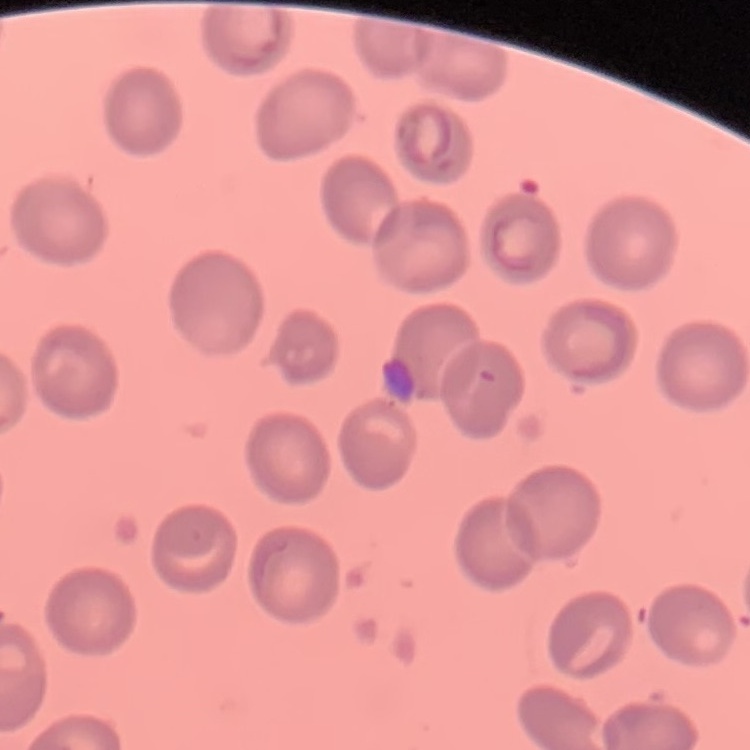

erythrocyte morphology = no rouleaux formation
stain = Field's or Giemsa
preparation = thin blood smear
image type = one tile cut from a larger photomicrograph